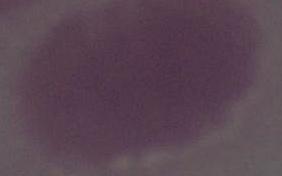
Summary:
  - Modality: micrograph
  - Identification: red blood cell
  - Magnification: 1000x